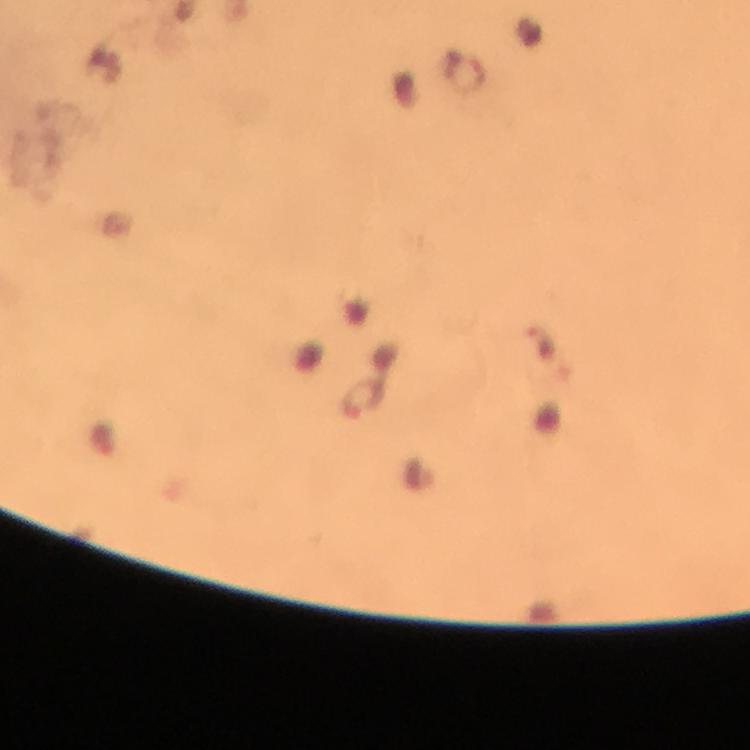

image size = 750×750 pixels
cropped from = a single field of view
context = from a malaria diagnostic workup
magnification = 100x
preparation = thick blood film
malaria parasite locations = approximate centers as [x, y] in pixels: [541, 344], [363, 399]
capture = smartphone photograph through a microscope
stain = Giemsa
immersion oil = applied